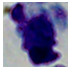 A leukocyte is seen. Photomicrograph. Captured at 1000x magnification.